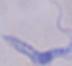

magnification = 1000x
identification = trypanosome
modality = photomicrograph